Comment on the morphology of the red blood cells.
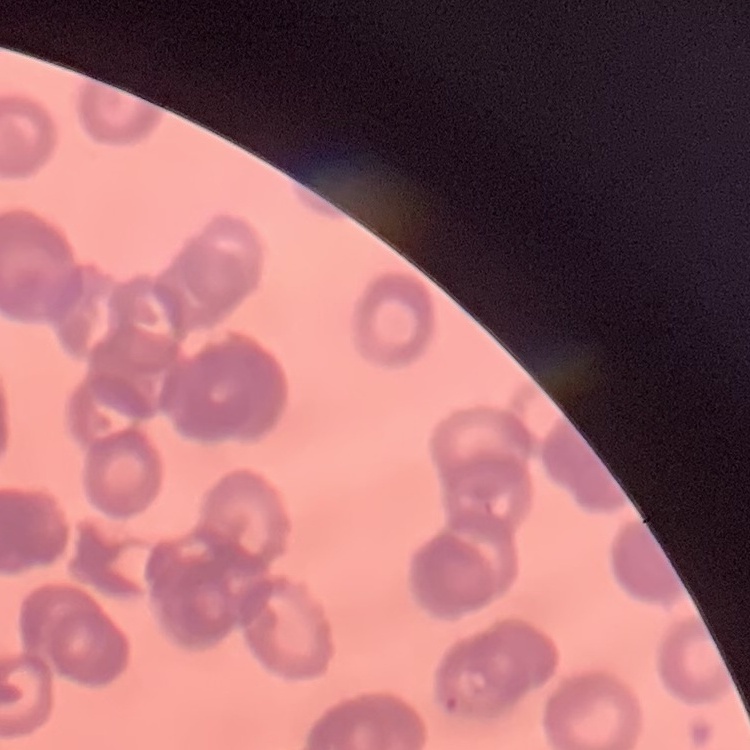

They show rouleaux formation.

Square crop of a larger photomicrograph. Stained with either Field's or Giemsa. Thin blood smear.